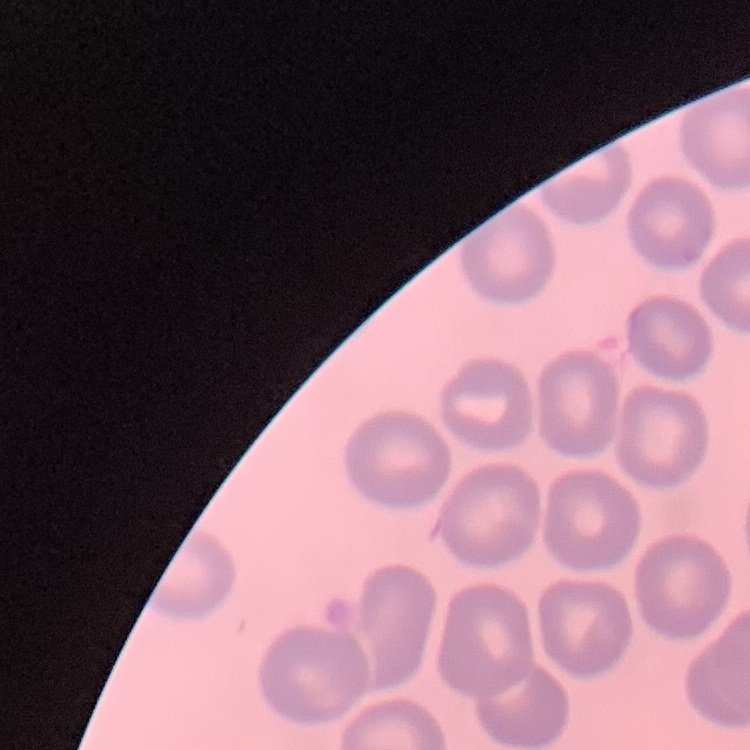
red blood cell morphology = no rouleaux formation
image type = square crop of a larger photomicrograph
stain = Field's or Giemsa
preparation = thin peripheral smear